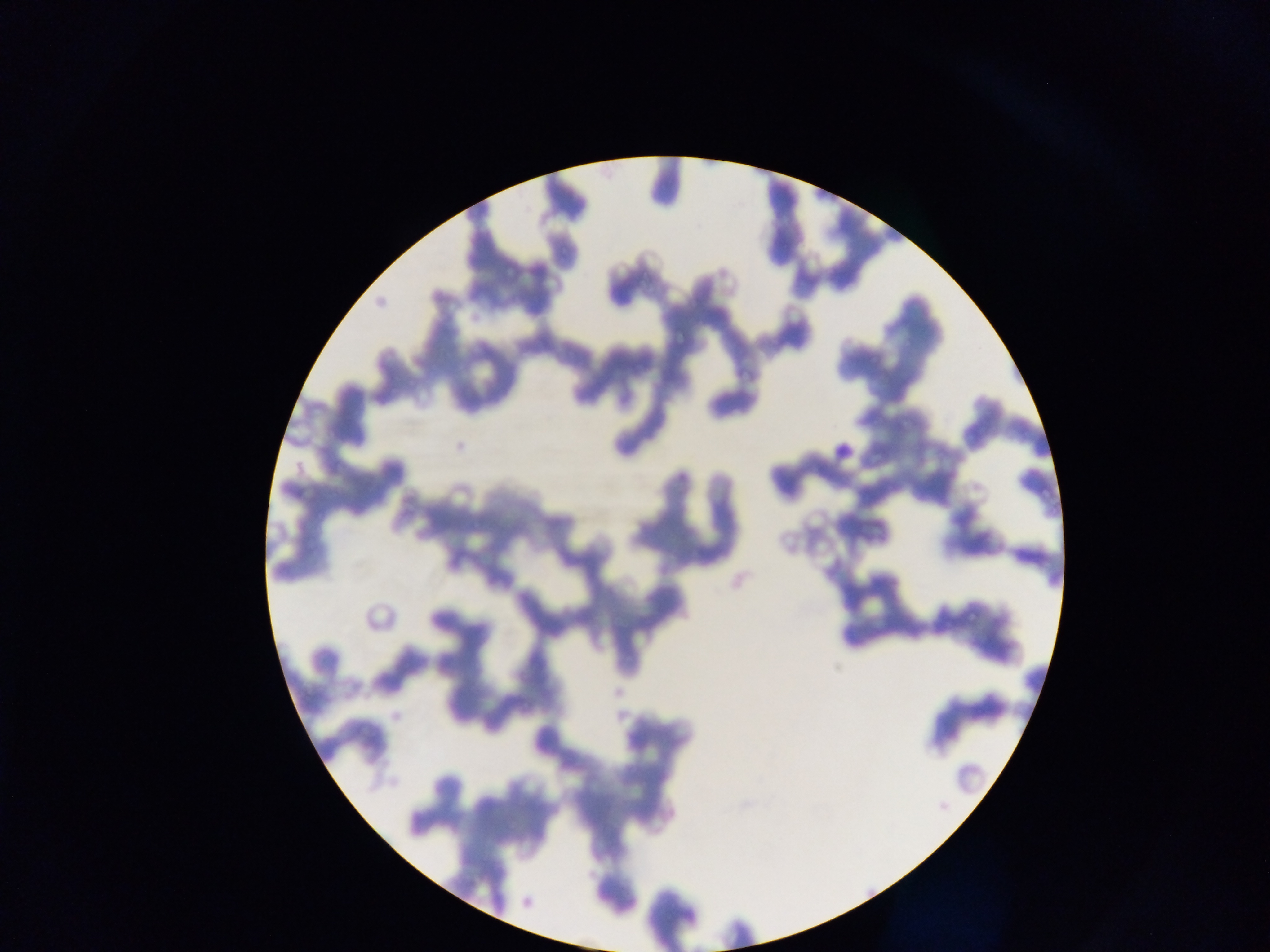

Approximate bounding boxes as {left, top, right, bottom} in pixels.
Summary:
  - Plasmodium parasite locations: {495, 258, 515, 278}, {666, 317, 694, 350}, {1017, 469, 1063, 507}
  - Field of view: single
  - Image size: 1270×952 pixels
  - Preparation: thin blood film
  - Country: Ghana
  - Capture: mobile-phone photograph through a microscope